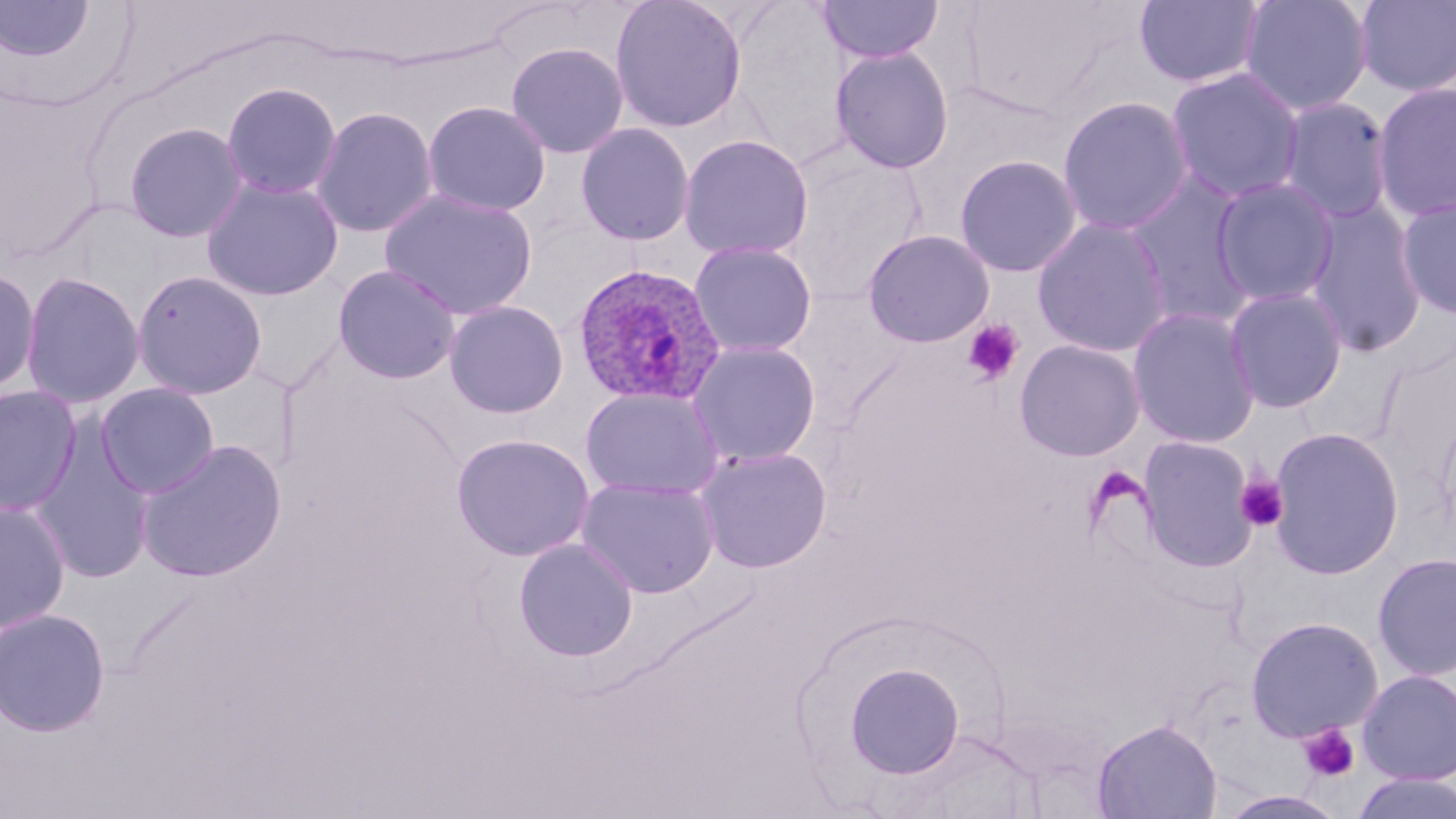

Summary:
  - Coordinate format: approximate bounding boxes as (x1, y1, x2, y2) in pixels
  - Plasmodium ovale-infected red blood cell locations: (573, 262, 727, 407)
  - Uninfected red blood cell locations: (609, 0, 747, 133), (725, 0, 858, 166), (1133, 0, 1266, 90), (1238, 0, 1374, 116), (1353, 0, 1455, 98), (817, 1, 944, 64), (0, 2, 96, 61), (1142, 4, 1283, 164), (506, 42, 629, 159), (830, 46, 954, 173), (1165, 67, 1306, 204), (220, 81, 343, 200), (1372, 81, 1456, 221), (1057, 95, 1195, 236), (1277, 96, 1393, 224), (422, 101, 551, 217), (311, 106, 439, 239), (122, 121, 250, 243), (575, 123, 695, 246), (678, 134, 814, 260), (784, 143, 926, 300), (954, 154, 1083, 277), (1122, 170, 1259, 327), (201, 177, 344, 301), (1210, 177, 1340, 307), (380, 188, 537, 320), (1395, 195, 1456, 320), (1302, 201, 1428, 358), (1032, 217, 1172, 358), (862, 230, 995, 348), (689, 241, 817, 359), (333, 264, 461, 384), (0, 266, 41, 399), (131, 269, 268, 399), (20, 271, 145, 409), (1223, 286, 1348, 413), (444, 299, 569, 419), (1127, 306, 1261, 449), (1014, 339, 1145, 461), (687, 341, 821, 467), (94, 382, 220, 498), (0, 384, 82, 516), (579, 386, 724, 501), (1267, 426, 1405, 580), (451, 433, 596, 562), (1137, 435, 1259, 572), (30, 437, 157, 583), (136, 440, 287, 583), (695, 447, 832, 572), (577, 477, 720, 598), (0, 499, 71, 635), (513, 538, 638, 662), (1372, 551, 1456, 681), (0, 607, 111, 736), (1245, 616, 1383, 742), (844, 662, 965, 779), (1357, 669, 1456, 785), (1092, 717, 1222, 819), (1350, 771, 1456, 819)
  - Platelet locations: (961, 319, 1025, 385), (1235, 475, 1289, 532), (1298, 723, 1361, 783)
  - Slide-level diagnosis: Plasmodium ovale
  - Stain: May-Grünwald-Giemsa
  - Magnification: 1000x
  - Image size: 1456×819 pixels
  - Modality: optical microscopy
  - Preparation: thin blood film
  - Field of view: one of a larger specimen